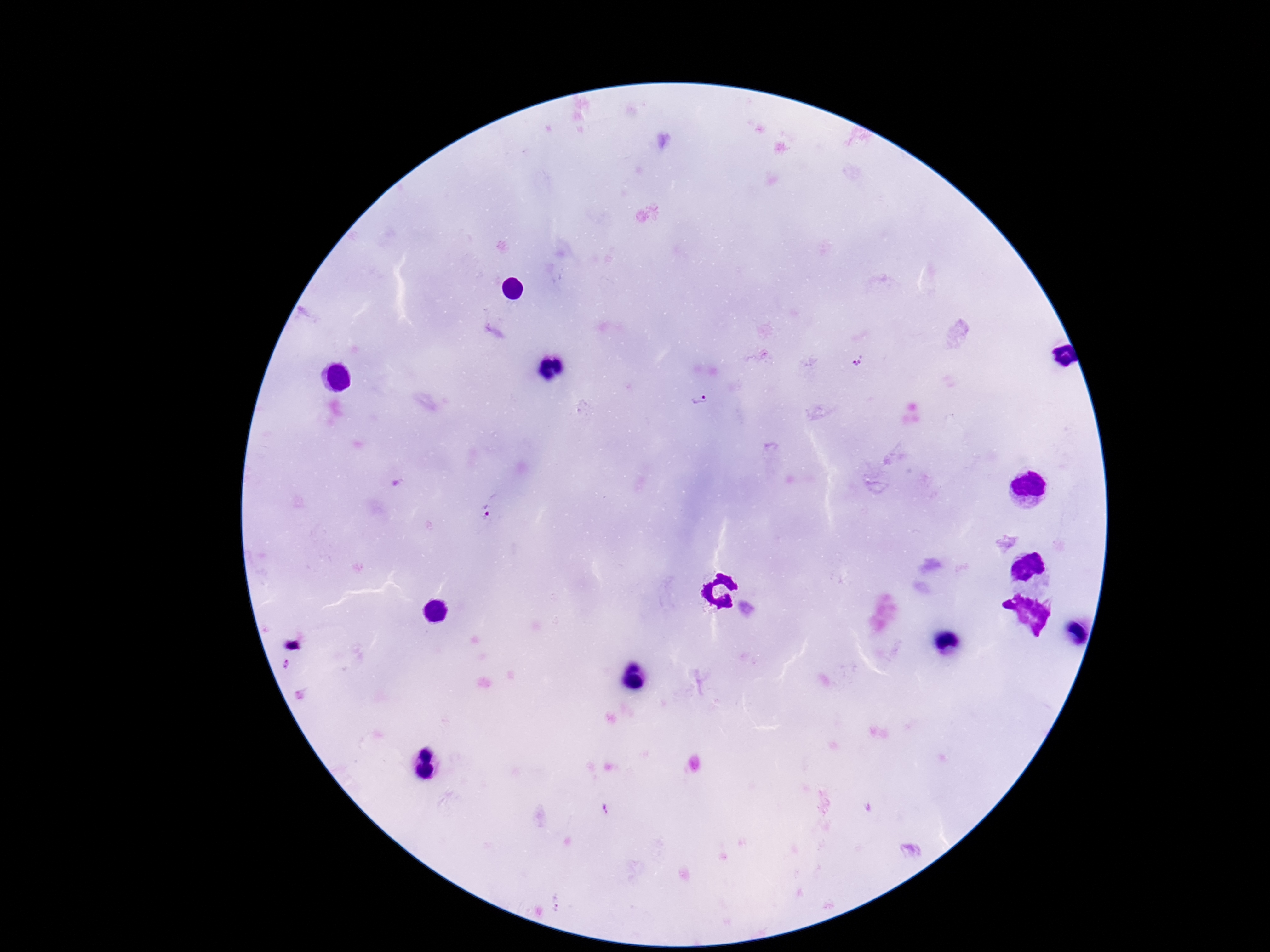
Approximate centers as [x, y] in pixels.
Summary:
  - Plasmodium parasite locations: [859, 359], [698, 401], [483, 513], [294, 640], [288, 665], [606, 808]
  - Capture: smartphone camera through the microscope eyepiece
  - Field of view: one from this slide
  - Patient malaria status: positive
  - Image size: 1270×952 pixels
  - Stain: Giemsa
  - Preparation: thick blood smear
  - Magnification: 100x